Classify this cell by malaria status.
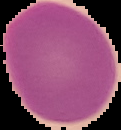

It is uninfected.

Image is 121×130 pixels. From a thin blood film. The area outside the segmented cell region is set to black.